Identify the preparation type.
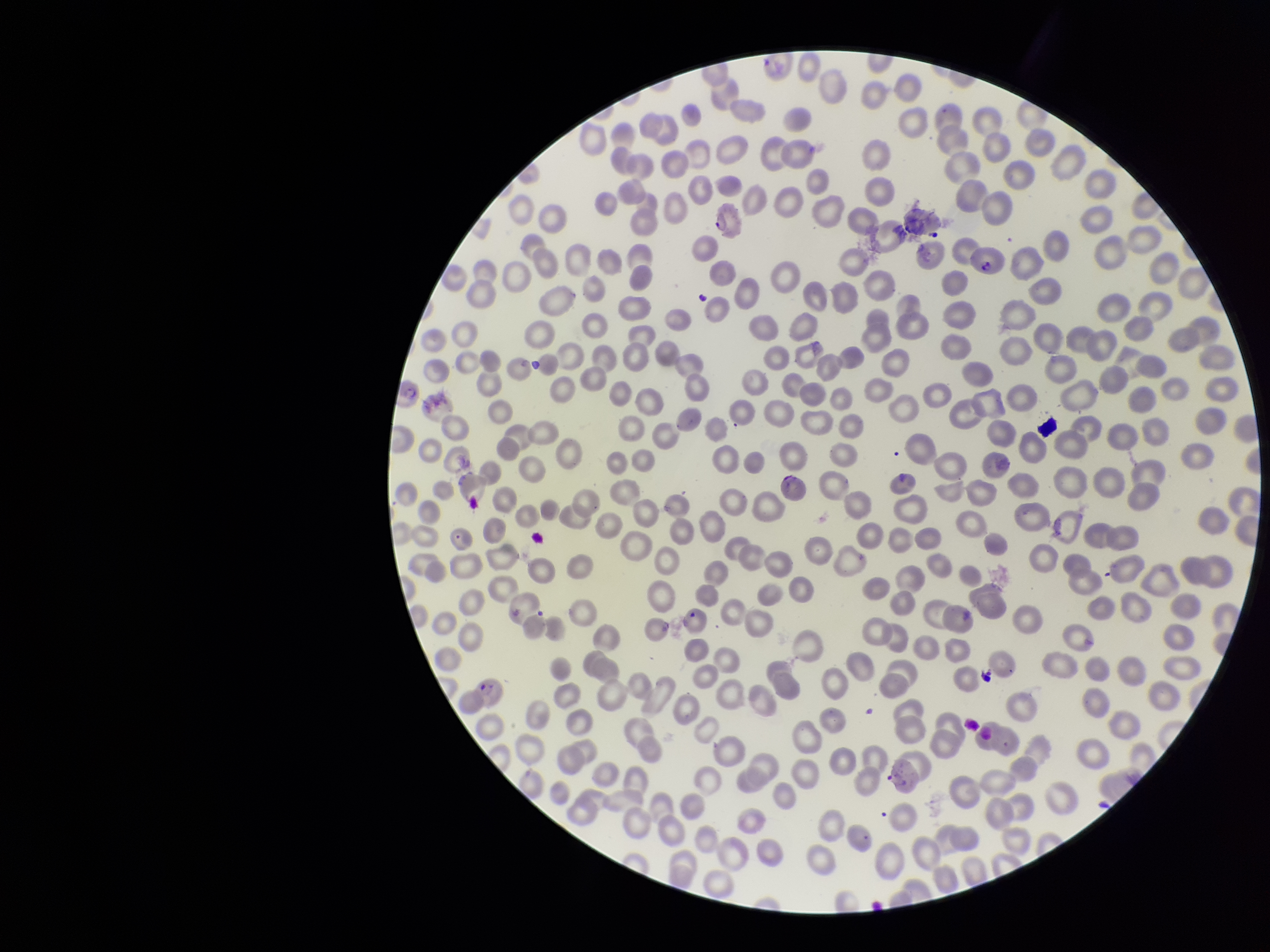
It is a thin blood smear.

parasitized red blood cell count = 1
species reported for this patient = Plasmodium falciparum
image size = 1270×952 pixels
stain = Giemsa
red blood cell count = 312
parasitized red blood cells = seen
capture = smartphone photograph through the microscope eyepiece
patient malaria status = infected
field of view = one from this slide